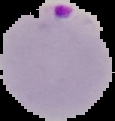

malaria_status: parasitized
image_type: segmented cell region with the area outside set to black
preparation: thin blood smear
image_size: 115×121 pixels